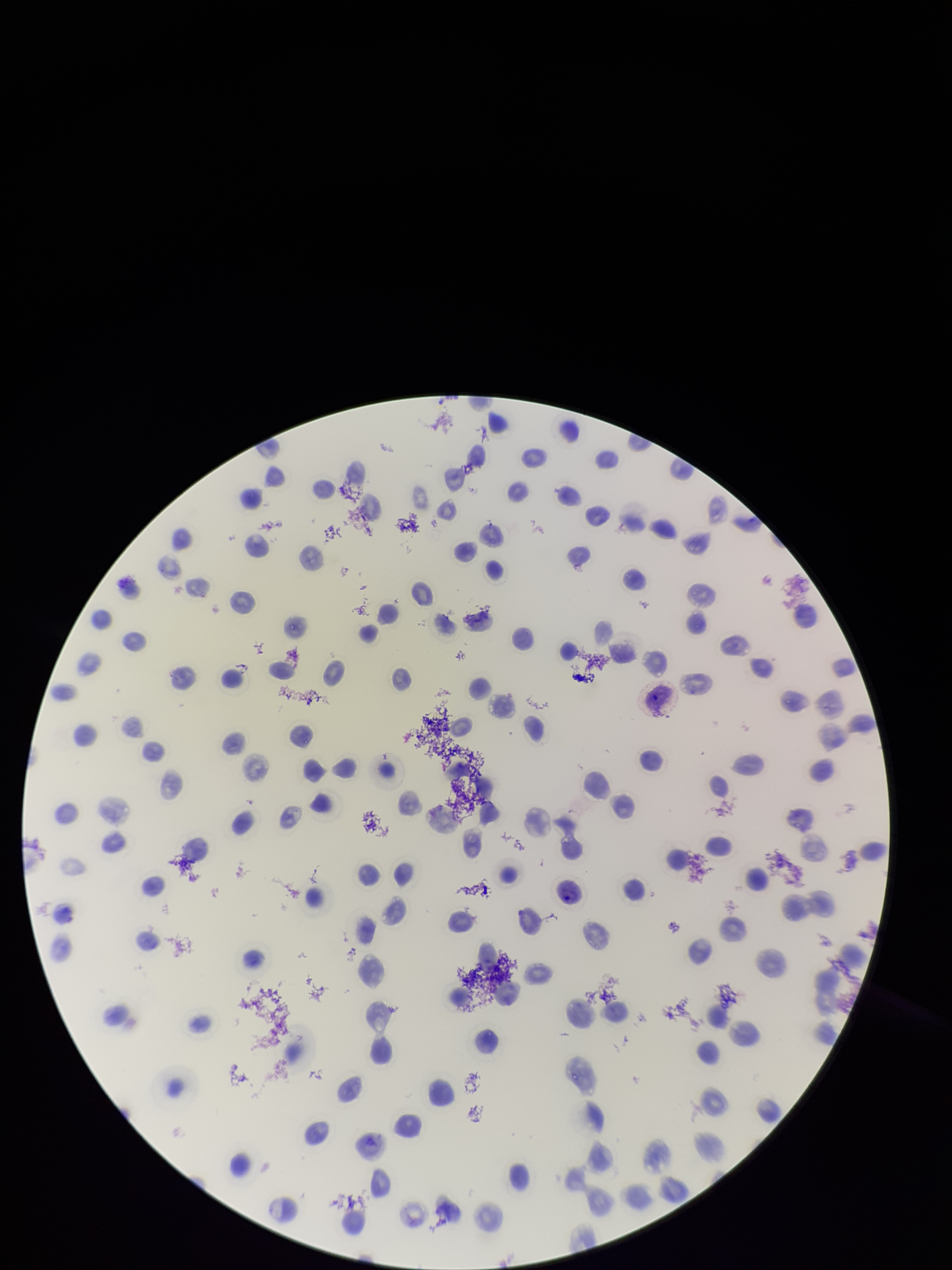
image size = 952×1270 pixels
patient malaria status = positive
species reported for this patient = Plasmodium vivax
stain = Giemsa
field of view = one from this slide
preparation = thin
red blood cell count = 109
capture = smartphone photograph through the microscope eyepiece
parasitized red blood cells = none seen
parasitized red blood cell count = 0